Report the malaria status of this cell.
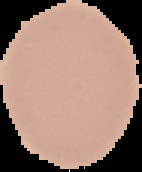

It is uninfected.

Summary:
  - Preparation: thin blood film
  - Image size: 142×172 pixels
  - Image type: segmented cell region with the area outside set to black